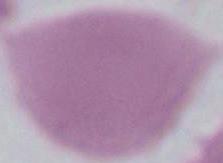

{
  "magnification": "1000x",
  "identification": "erythrocyte",
  "modality": "micrograph"
}